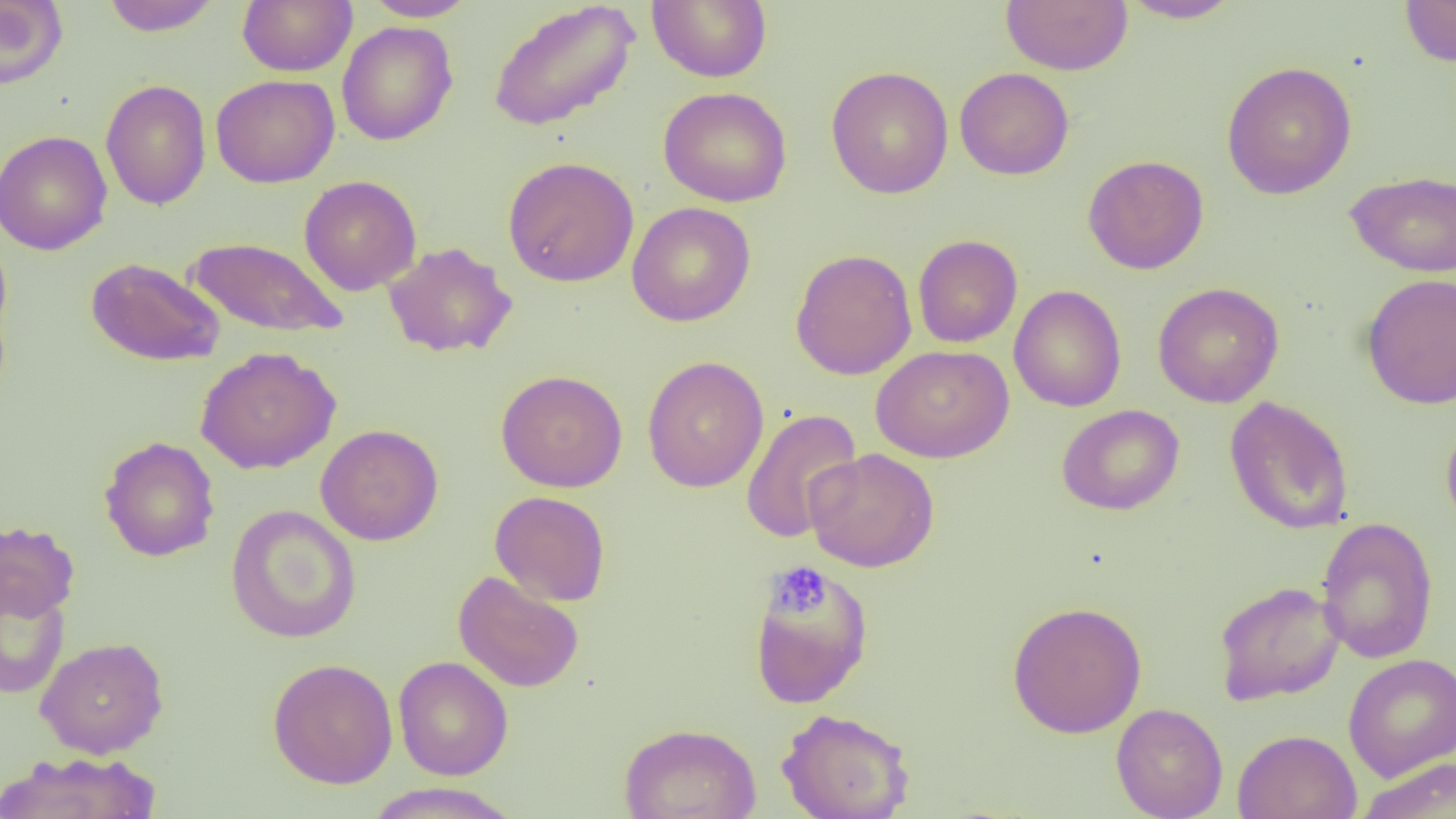
Summary:
  - Coordinate format: approximate bounding boxes as [x1, y1, x2, y2] in pixels
  - Uninfected red blood cell locations: [0, 0, 67, 89], [100, 0, 221, 36], [237, 0, 357, 76], [362, 0, 477, 21], [486, 0, 640, 133], [647, 0, 772, 83], [1001, 0, 1132, 75], [1119, 0, 1243, 23], [1399, 0, 1456, 66], [337, 21, 458, 145], [1221, 60, 1357, 200], [826, 66, 953, 199], [954, 67, 1074, 180], [211, 74, 340, 188], [100, 79, 211, 210], [658, 86, 793, 207], [0, 130, 112, 255], [1083, 154, 1209, 275], [502, 156, 639, 286], [1345, 170, 1456, 278], [299, 175, 421, 295], [626, 201, 756, 327], [0, 232, 13, 344], [913, 234, 1023, 348], [187, 237, 347, 339], [383, 242, 518, 358], [790, 248, 917, 380], [86, 257, 224, 367], [1361, 273, 1456, 409], [1152, 282, 1284, 408], [1010, 285, 1126, 412], [871, 344, 1013, 463], [195, 346, 340, 474], [642, 355, 769, 493], [496, 369, 628, 493], [1224, 396, 1354, 535], [1057, 404, 1185, 516], [741, 408, 863, 543], [1441, 416, 1456, 537], [315, 424, 444, 546], [99, 436, 221, 562], [804, 448, 940, 572], [489, 490, 611, 606], [225, 504, 362, 644], [1315, 517, 1439, 664], [0, 519, 79, 621], [747, 561, 874, 710], [452, 570, 584, 693], [1214, 580, 1346, 705], [0, 581, 70, 698], [1007, 600, 1147, 738], [35, 636, 169, 758], [1343, 653, 1456, 780], [393, 656, 513, 780], [267, 658, 398, 789], [1111, 703, 1228, 819], [776, 708, 915, 819], [619, 722, 761, 819], [1233, 729, 1362, 819], [0, 752, 160, 818], [1358, 757, 1456, 819], [365, 782, 520, 818]
  - Platelet locations: [769, 562, 831, 618]
  - Slide-level diagnosis: negative for blood parasites
  - Magnification: 1000x
  - Preparation: thin blood film
  - Image size: 1456×819 pixels
  - Modality: optical microscopy
  - Field of view: single